Outline each Plasmodium vivax-infected red blood cell.
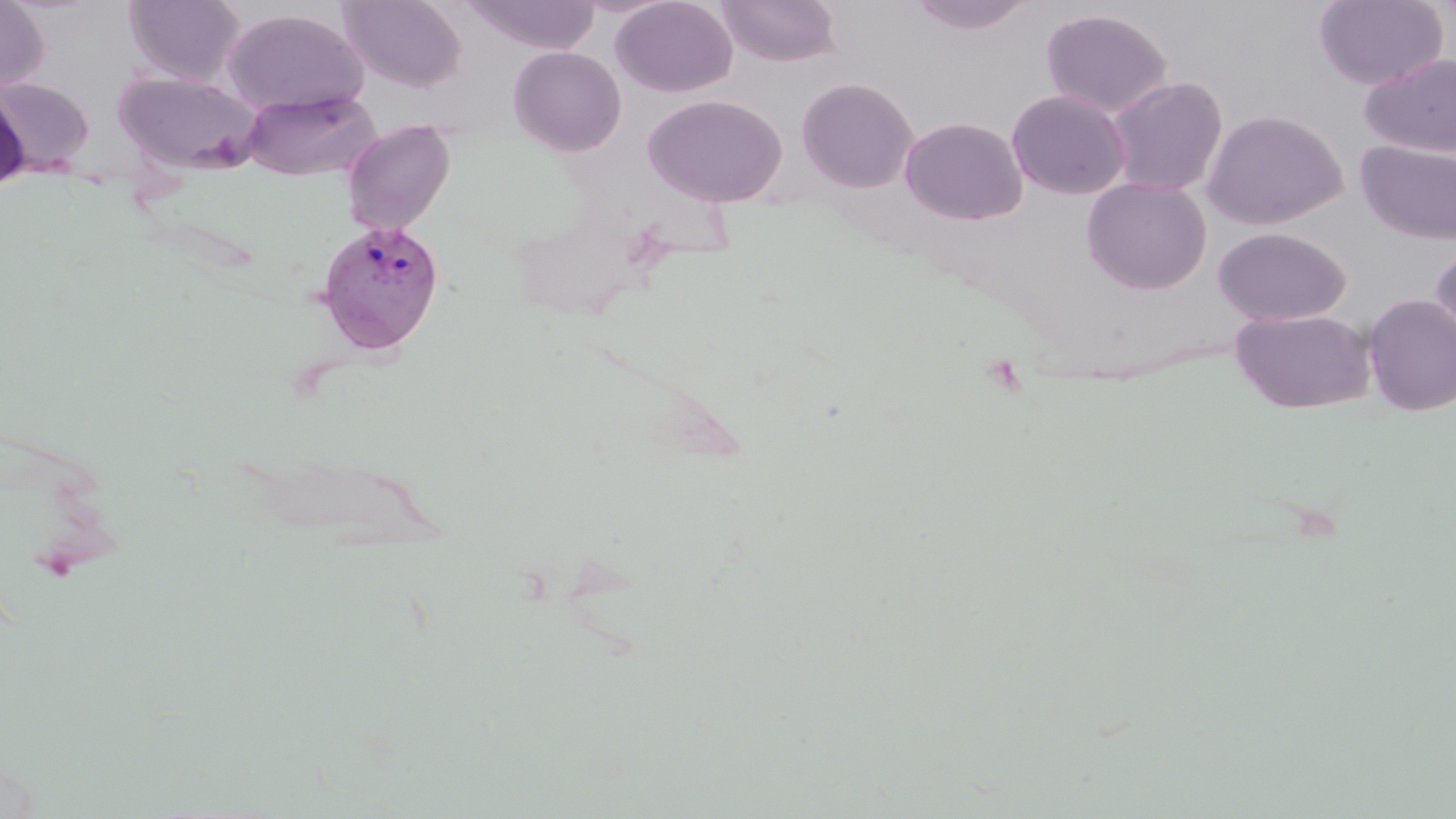
Approximate bounding boxes as (x1, y1, x2, y2) in pixels.
Plasmodium vivax-infected red blood cells: (314, 219, 447, 356).

slide_level_diagnosis: Plasmodium vivax
field_of_view: single
uninfected_red_blood_cell_locations: 'approximate bounding boxes as (x1, y1, x2, y2) in pixels: (0, 0, 49, 92), (124, 0, 245, 86), (339, 0, 466, 92), (461, 0, 602, 54), (611, 0, 738, 97), (716, 0, 842, 67), (906, 0, 1035, 35), (1314, 0, 1448, 90), (222, 8, 368, 115), (1040, 8, 1173, 118), (509, 45, 626, 156), (1359, 52, 1456, 158), (113, 69, 266, 175), (0, 74, 95, 173), (1106, 76, 1227, 196), (796, 77, 918, 193), (0, 86, 31, 193), (241, 89, 380, 181), (1006, 89, 1131, 200), (642, 94, 787, 207), (1202, 108, 1348, 230), (899, 116, 1028, 225), (341, 119, 456, 234), (1355, 139, 1456, 245), (1081, 177, 1212, 295), (1212, 227, 1352, 326), (1429, 240, 1456, 350), (1363, 294, 1456, 417), (1231, 308, 1377, 414)'
preparation: thin blood smear
magnification: 1000x
image_size: 1456×819 pixels
modality: optical microscopy
stain: May-Grünwald-Giemsa